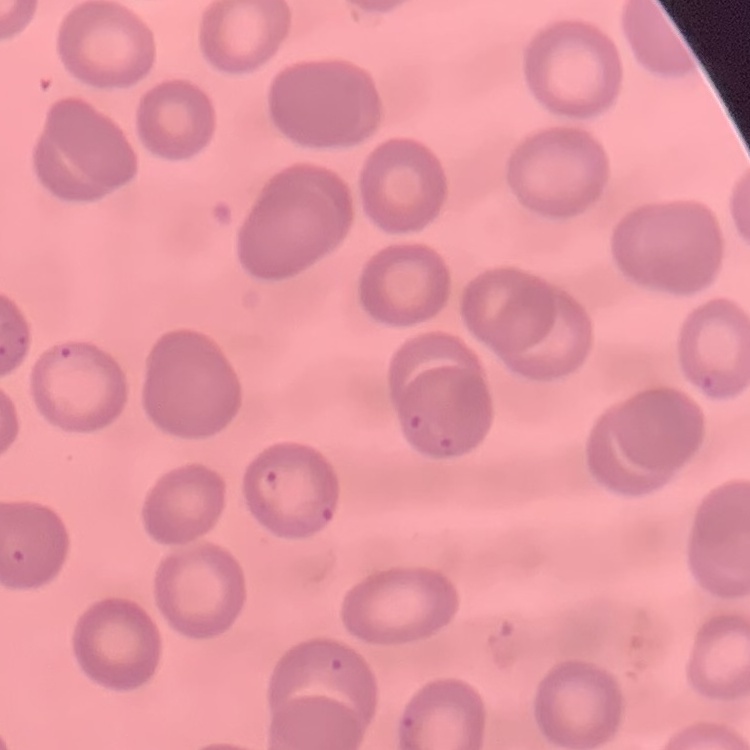
The erythrocytes exhibit no rouleaux formation. Stained with either Field's or Giemsa. Square crop of a larger photomicrograph. Thin peripheral smear.